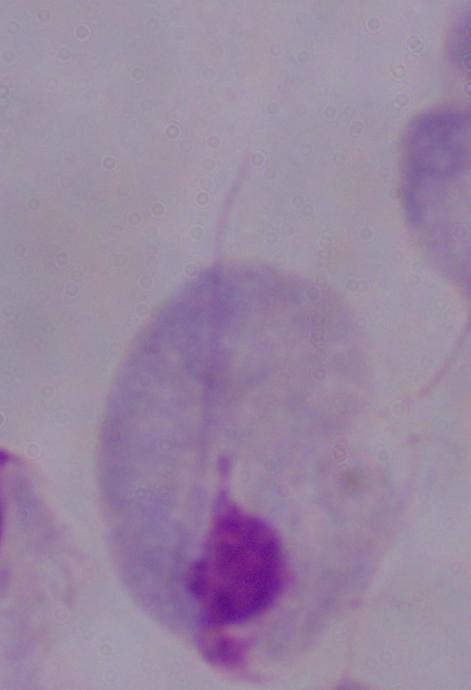
magnification = 1000x
modality = micrograph
identification = trichomonad